Assess this cell for malaria.
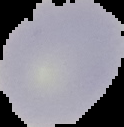

It is uninfected.

Segmented cell region on a black background. Image is 124×127 pixels. From a thin blood smear.